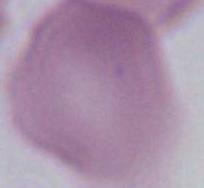

Summary:
  - Magnification: 1000x
  - Identification: erythrocyte
  - Modality: micrograph